Describe the morphology of the erythrocytes.
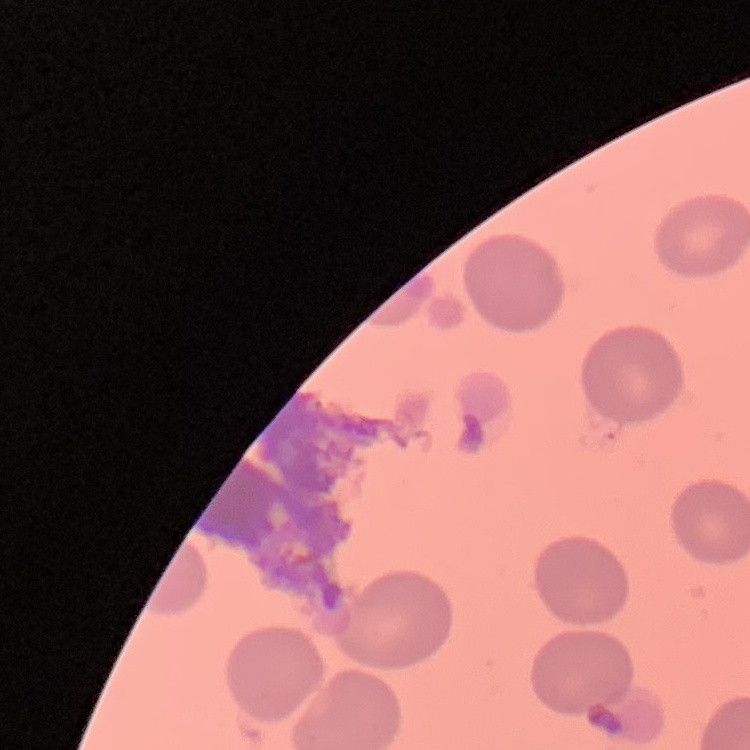
No rouleaux formation.

Square crop of a larger photomicrograph. Stained with either Field's or Giemsa. Thin blood film.